Point out each malaria parasite.
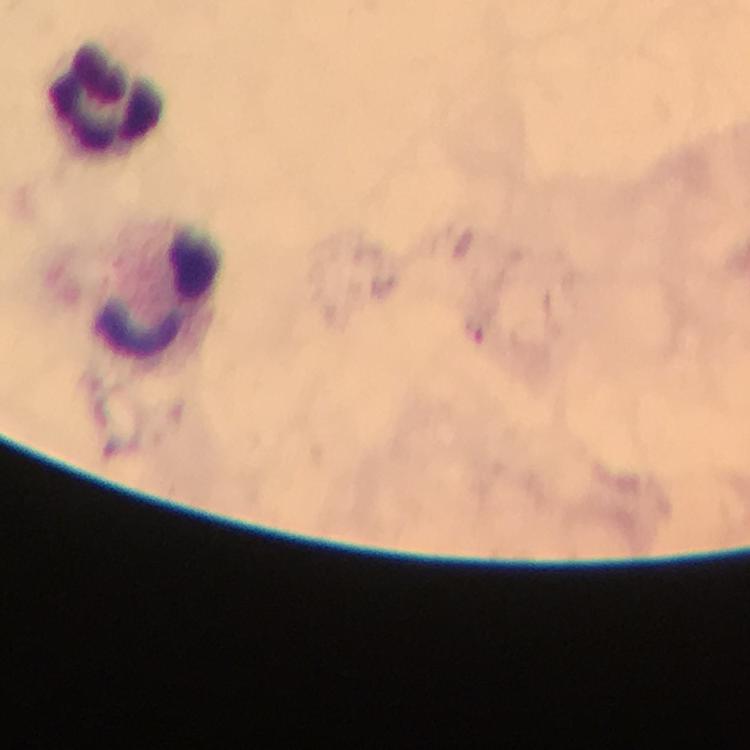
No malaria parasites seen.

preparation: thick smear
context: from a malaria diagnostic workup
capture: smartphone mounted on the microscope
leukocyte_locations: 'approximate object centers, in pixels from the top-left corner: (x=105, y=94), (x=157, y=290)'
stain: Giemsa
immersion_oil: used
magnification: 100x
cropped_from: one field of view
image_size: 750×750 pixels